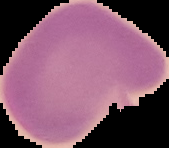
Summary:
  - Image size: 169×148 pixels
  - Preparation: thin blood film
  - Image type: segmented cell region on a black background
  - Result: no malaria parasites detected